Identify the preparation type.
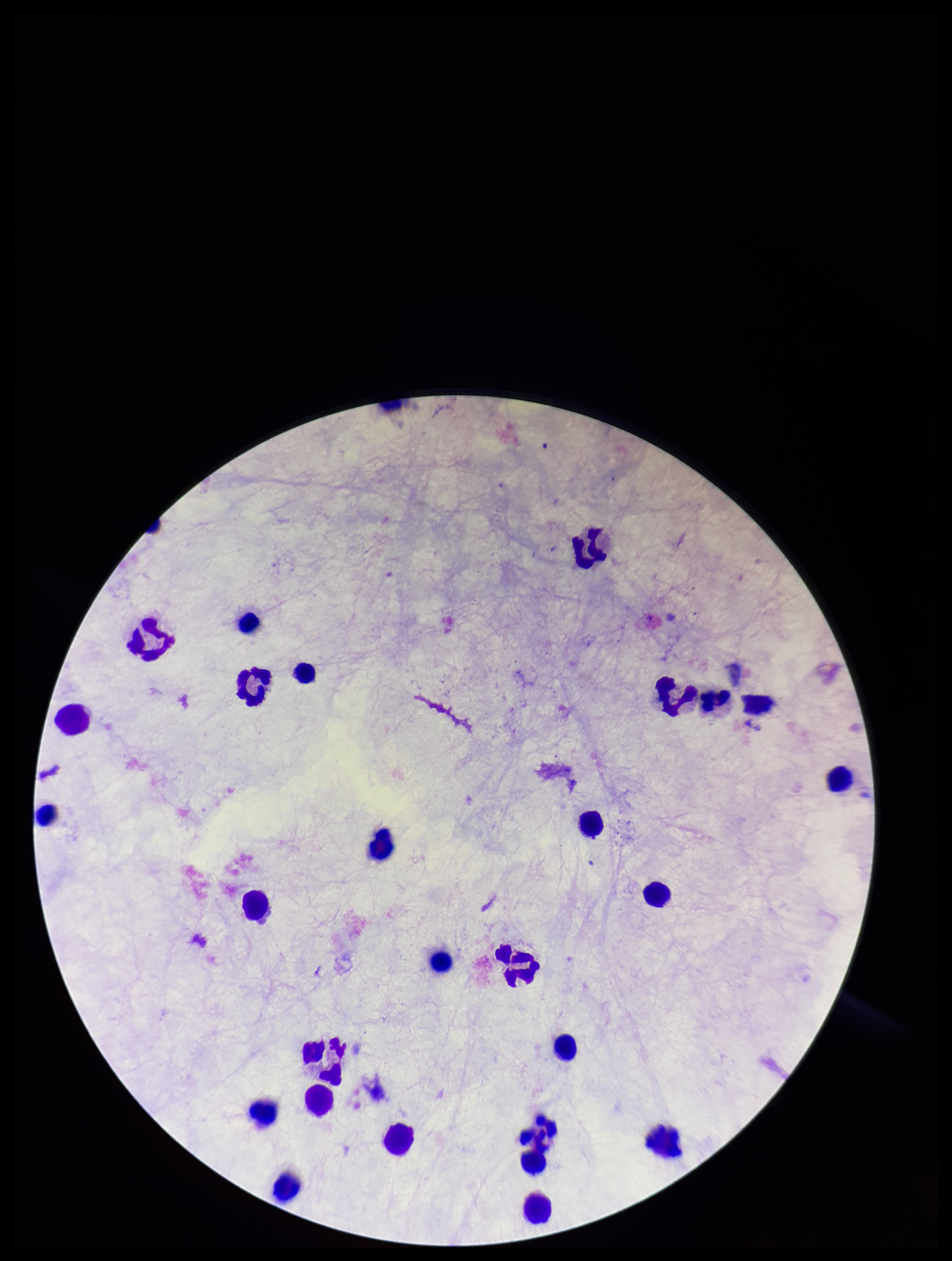
It is a thick blood smear.

Patient malaria status: negative. Parasite count: 0. Leukocyte count: 26. Image is 952×1261 pixels. Single field of view. Giemsa stain. Photographed through the microscope eyepiece with a smartphone camera. Plasmodium parasites: none identified.